Comment on the morphology of the erythrocytes.
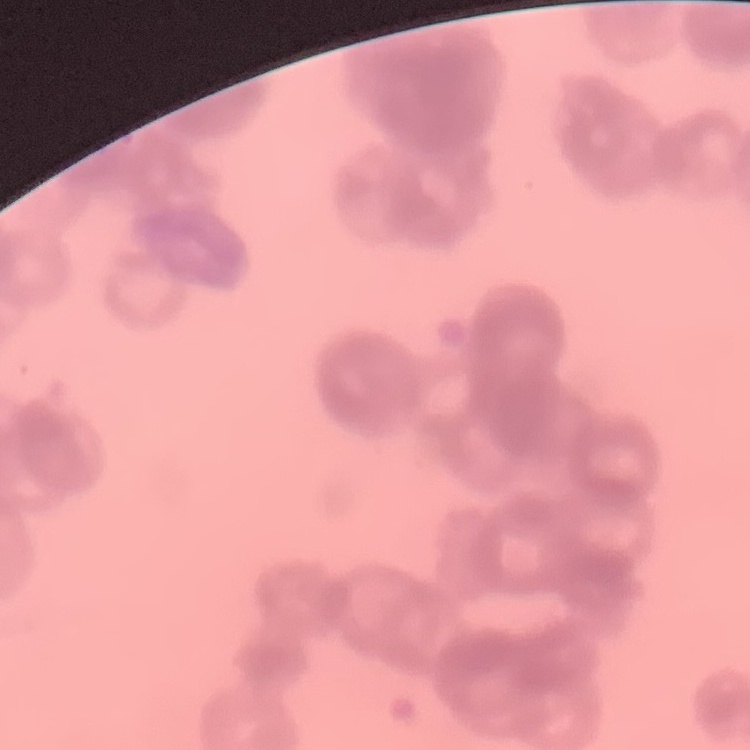
They show rouleaux formation.

One tile cut from a larger photomicrograph. Stained with either Field's or Giemsa. Thin blood film.